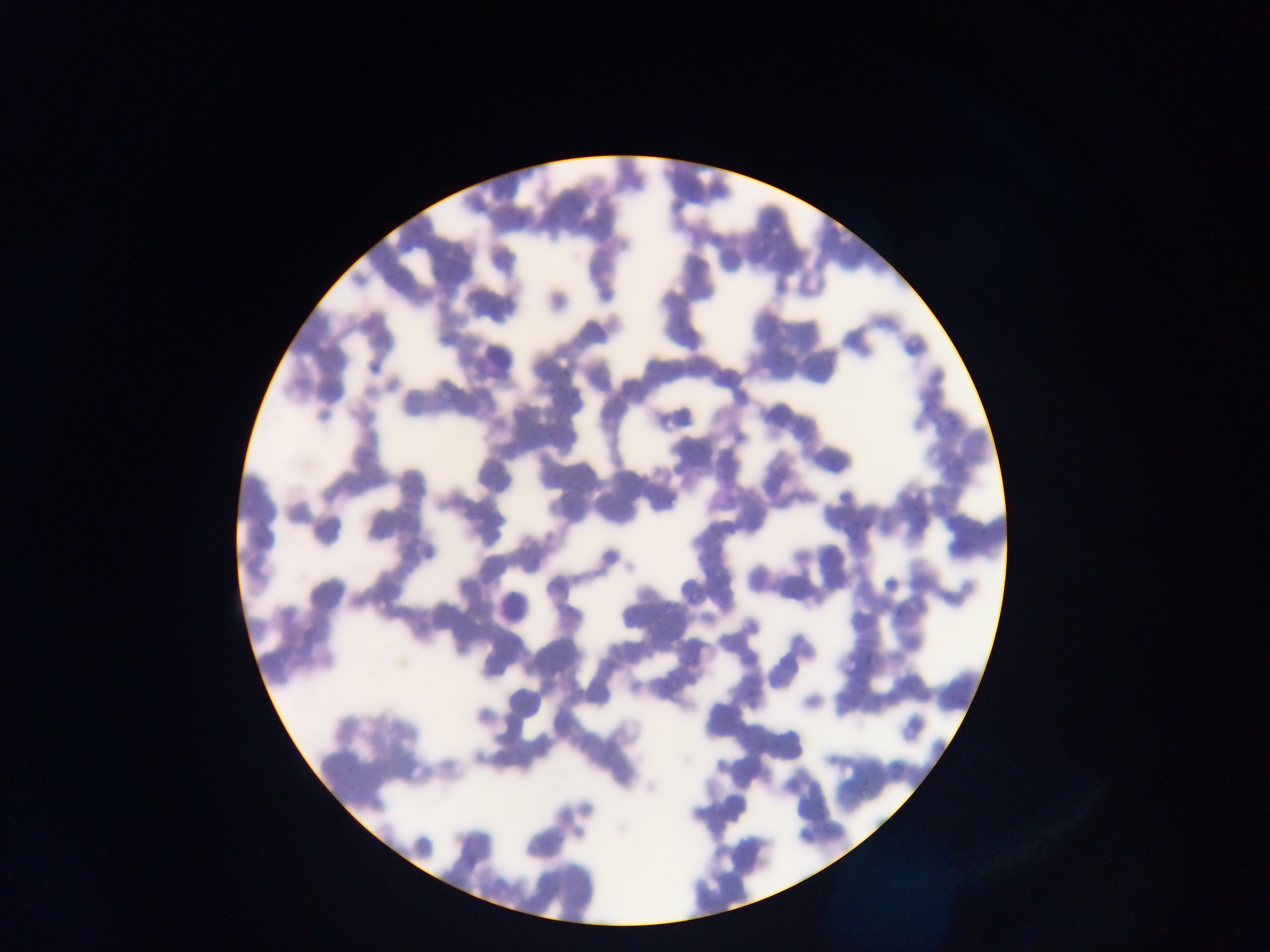
leukocyte locations = approximate bounding boxes as [left, top, right, bottom] in pixels: [479, 332, 519, 372]
country = Ghana
malaria parasite locations = approximate bounding boxes as [left, top, right, bottom] in pixels: [562, 367, 572, 375], [558, 378, 571, 394], [916, 398, 941, 413], [556, 402, 571, 412], [945, 410, 953, 420], [851, 510, 866, 532], [866, 653, 874, 664], [859, 671, 873, 690]
preparation = thin blood smear
capture = mobile-phone photograph through a microscope
image size = 1270×952 pixels
field of view = single